Assess this cell for malaria.
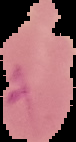
It is parasitized.

Image is 76×142 pixels. From a thin blood film. Cell region segmented out of the field of view; the surrounding area is masked to black.